Report the malaria status of this cell.
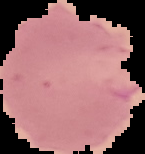

It is parasitized.

From a thin blood film. The area outside the segmented cell region is set to black. Image is 145×154 pixels.